Locate every Plasmodium parasite.
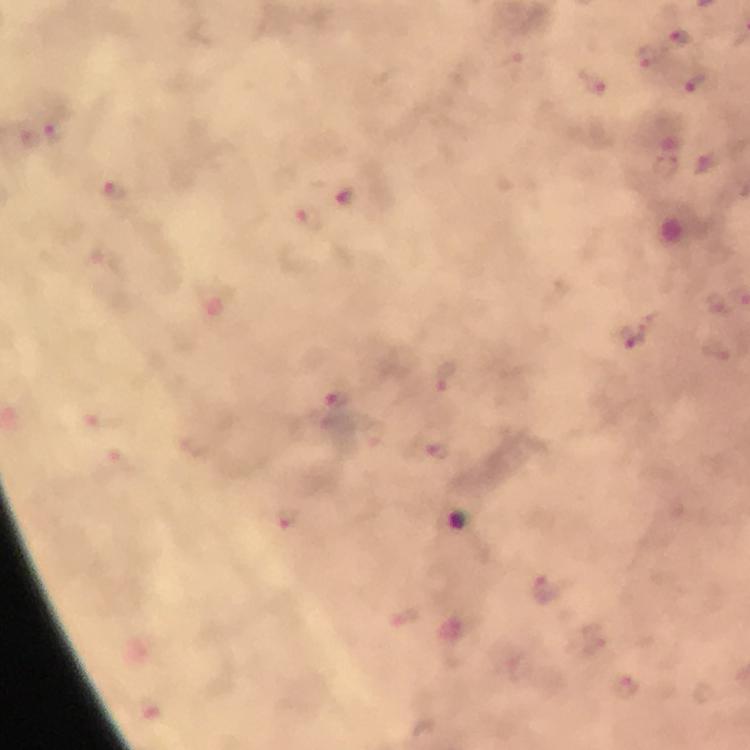
Approximate centers as {x, y} in pixels.
Plasmodium parasites: {680, 38}, {55, 127}, {121, 194}, {311, 218}, {632, 338}, {335, 406}, {626, 686}.

Summary:
  - Image size: 750×750 pixels
  - Stain: Giemsa
  - Capture: smartphone mounted on the microscope
  - Magnification: 100x
  - Preparation: thick smear
  - Cropped from: a single field of view
  - Immersion oil: applied
  - Context: from a diagnostic examination for malaria